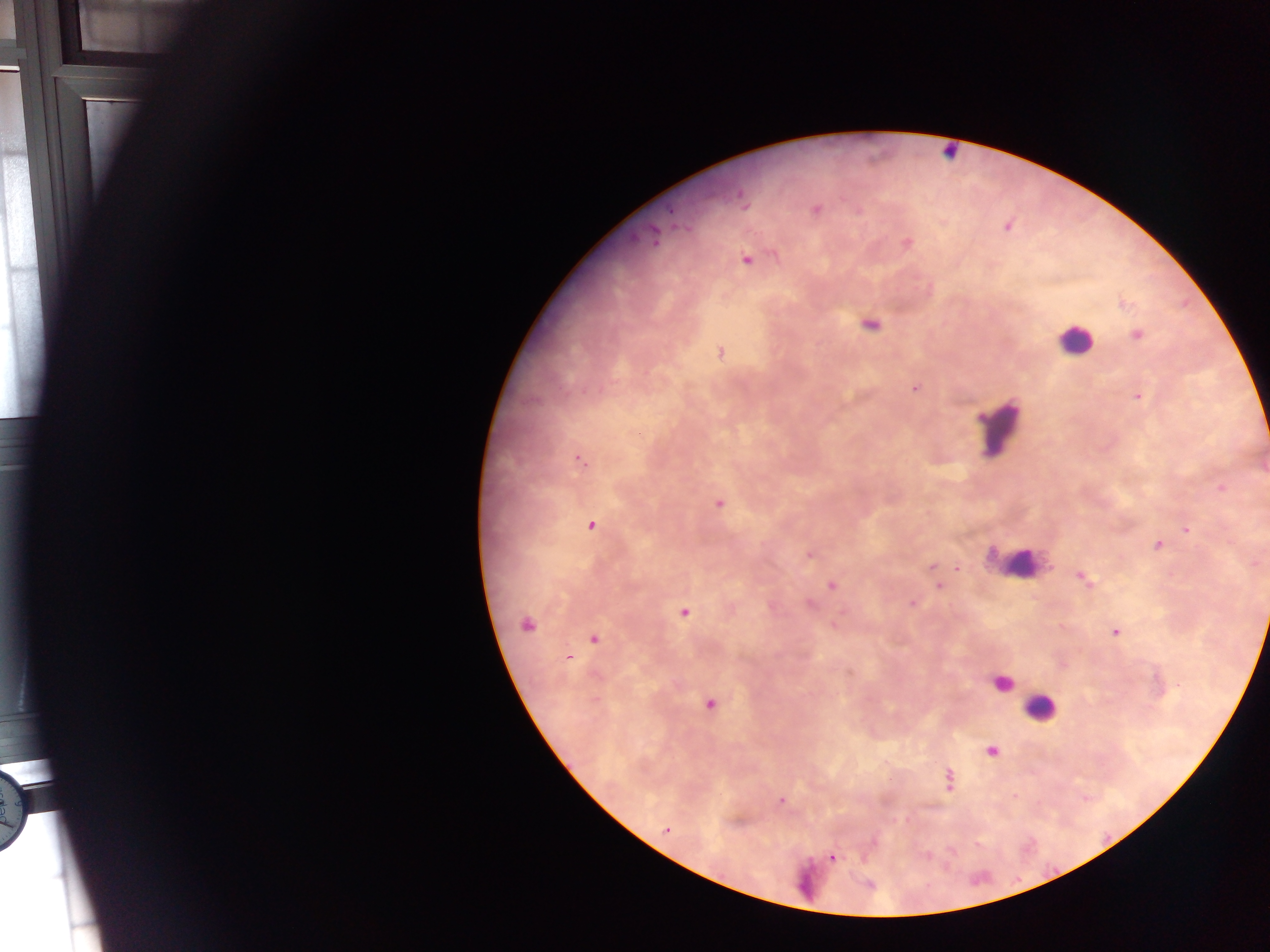
leukocyte_locations: 'approximate centers as {x, y} in pixels: {949, 151}, {1075, 341}, {999, 430}, {1017, 563}, {1000, 683}, {1050, 707}, {800, 875}'
malaria_parasite_locations: 'approximate centers as {x, y} in pixels: {741, 194}, {815, 210}, {1007, 225}, {652, 237}, {906, 243}, {746, 259}, {1123, 303}, {869, 323}, {1136, 335}, {720, 352}, {916, 388}, {1137, 396}, {637, 433}, {578, 459}, {1221, 486}, {718, 502}, {590, 525}, {1186, 529}, {1157, 545}, {810, 553}, {932, 566}, {957, 567}, {1082, 576}, {831, 585}, {939, 585}, {912, 603}, {808, 604}, {684, 612}, {526, 623}, {835, 624}, {1115, 631}, {593, 638}, {567, 657}, {1179, 685}, {709, 703}, {991, 750}, {948, 780}, {1013, 798}, {780, 801}, {666, 830}, {832, 857}'
country: Ghana
capture: mobile-phone photograph through a microscope
field_of_view: single
image_size: 1270×952 pixels
preparation: thick blood film